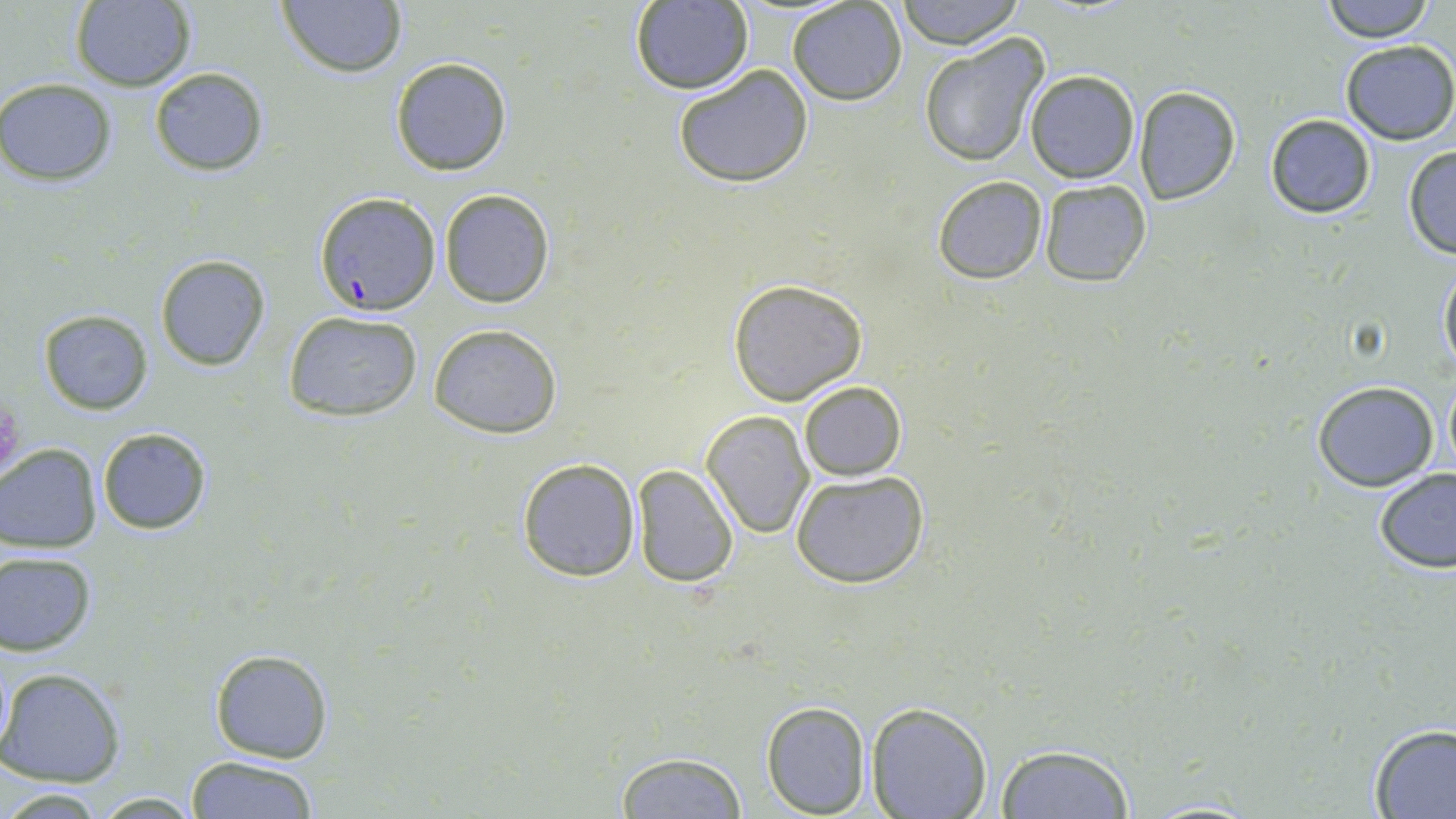 Approximate bounding boxes as named x1/y1/x2/y2 corners in pixels. Plasmodium falciparum-infected red blood cell locations: (x1=314, y1=192, x2=442, y2=316). Uninfected red blood cell locations: (x1=894, y1=0, x2=1025, y2=50), (x1=1319, y1=0, x2=1437, y2=42), (x1=68, y1=1, x2=196, y2=91), (x1=275, y1=1, x2=408, y2=79), (x1=628, y1=1, x2=754, y2=95), (x1=787, y1=1, x2=907, y2=106), (x1=919, y1=35, x2=1049, y2=168), (x1=1338, y1=40, x2=1455, y2=146), (x1=390, y1=57, x2=512, y2=176), (x1=148, y1=65, x2=269, y2=176), (x1=673, y1=65, x2=815, y2=189), (x1=1025, y1=70, x2=1139, y2=183), (x1=0, y1=77, x2=118, y2=187), (x1=1133, y1=86, x2=1242, y2=205), (x1=1265, y1=113, x2=1376, y2=219), (x1=1401, y1=145, x2=1456, y2=258), (x1=933, y1=175, x2=1048, y2=283), (x1=1038, y1=178, x2=1152, y2=287), (x1=440, y1=188, x2=556, y2=308), (x1=155, y1=254, x2=269, y2=372), (x1=1438, y1=259, x2=1456, y2=376), (x1=728, y1=277, x2=870, y2=406), (x1=37, y1=309, x2=155, y2=416), (x1=283, y1=310, x2=424, y2=422), (x1=428, y1=324, x2=563, y2=439), (x1=1442, y1=374, x2=1455, y2=480), (x1=1312, y1=381, x2=1440, y2=492), (x1=800, y1=382, x2=907, y2=481), (x1=701, y1=410, x2=814, y2=538), (x1=95, y1=426, x2=213, y2=535), (x1=0, y1=443, x2=102, y2=554), (x1=516, y1=457, x2=640, y2=581), (x1=631, y1=464, x2=739, y2=588), (x1=1374, y1=469, x2=1456, y2=575), (x1=790, y1=470, x2=930, y2=589), (x1=0, y1=549, x2=98, y2=657), (x1=208, y1=647, x2=333, y2=764), (x1=0, y1=667, x2=127, y2=788), (x1=760, y1=700, x2=872, y2=817), (x1=867, y1=703, x2=992, y2=819), (x1=1367, y1=723, x2=1456, y2=818), (x1=993, y1=743, x2=1137, y2=819), (x1=615, y1=750, x2=747, y2=818), (x1=183, y1=755, x2=321, y2=819), (x1=86, y1=790, x2=204, y2=816), (x1=1129, y1=798, x2=1265, y2=818). Platelet locations: (x1=0, y1=397, x2=24, y2=477). Slide-level diagnosis: Plasmodium falciparum. Image is 1456×819 pixels. Single field of view. May-Grünwald-Giemsa stain. Thin blood film. 1000x magnification. Light microscopy.